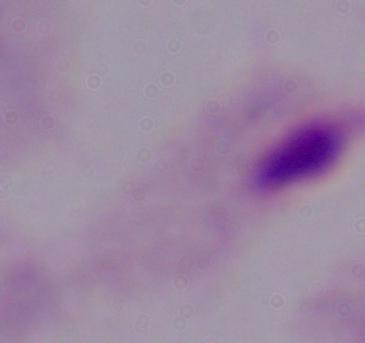
Summary:
  - Magnification: 1000x
  - Modality: photomicrograph
  - Identification: trichomonad